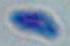
Summary:
  - Modality: micrograph
  - Magnification: 1000x
  - Identification: Toxoplasma gondii